Look for Plasmodium parasites.
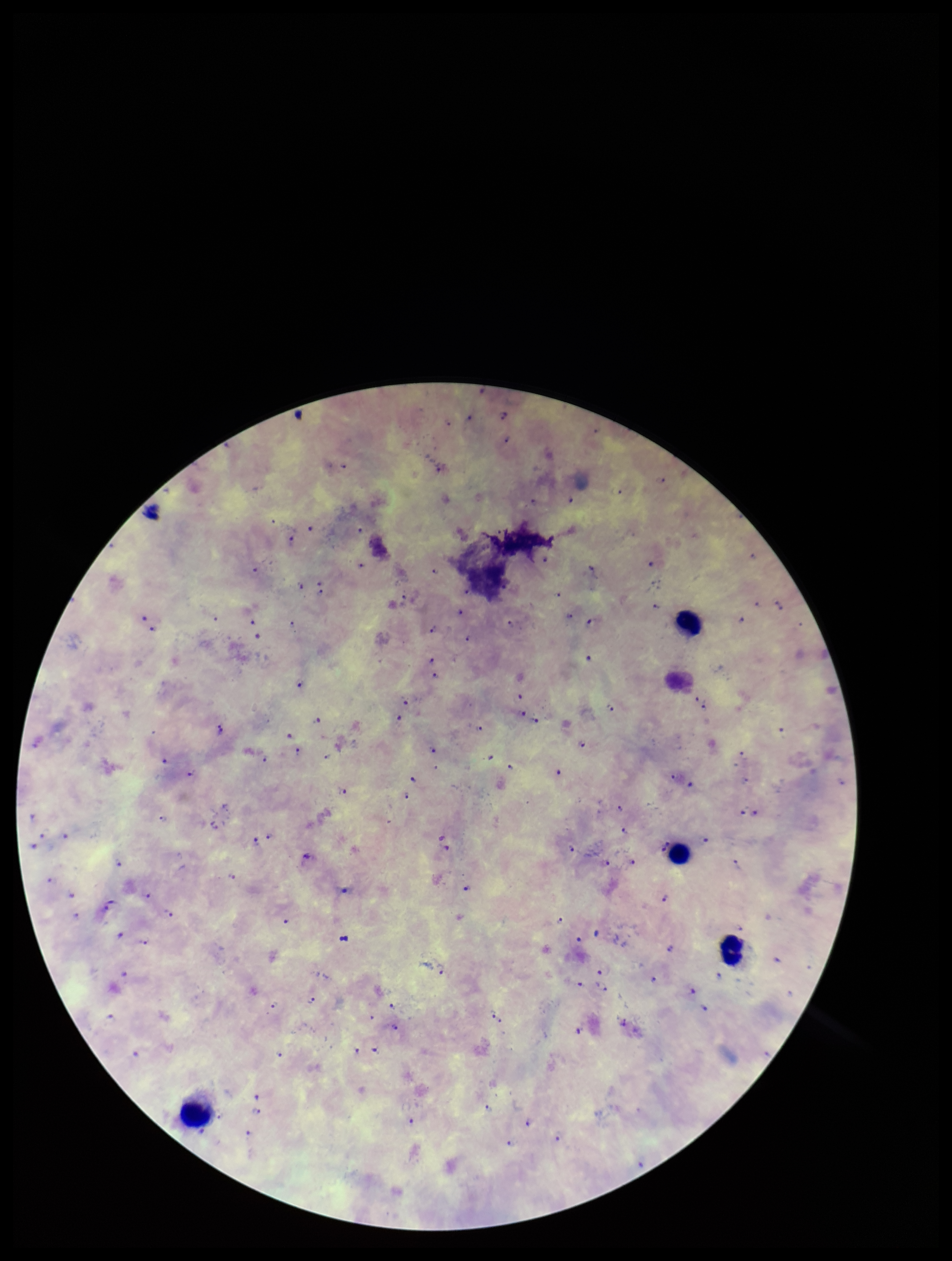
Detected.

Image is 952×1261 pixels. Leukocyte count: 4. Patient malaria status: infected. Smartphone photograph taken through the eyepiece of a microscope. Parasite count: 102. One field from this slide. Giemsa stain. Preparation: thick smear. Species reported for this patient: Plasmodium falciparum.